Identify the parasite.
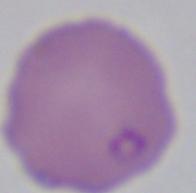

Babesia.

Summary:
  - Modality: photomicrograph
  - Magnification: 1000x